Describe the morphology of the erythrocytes.
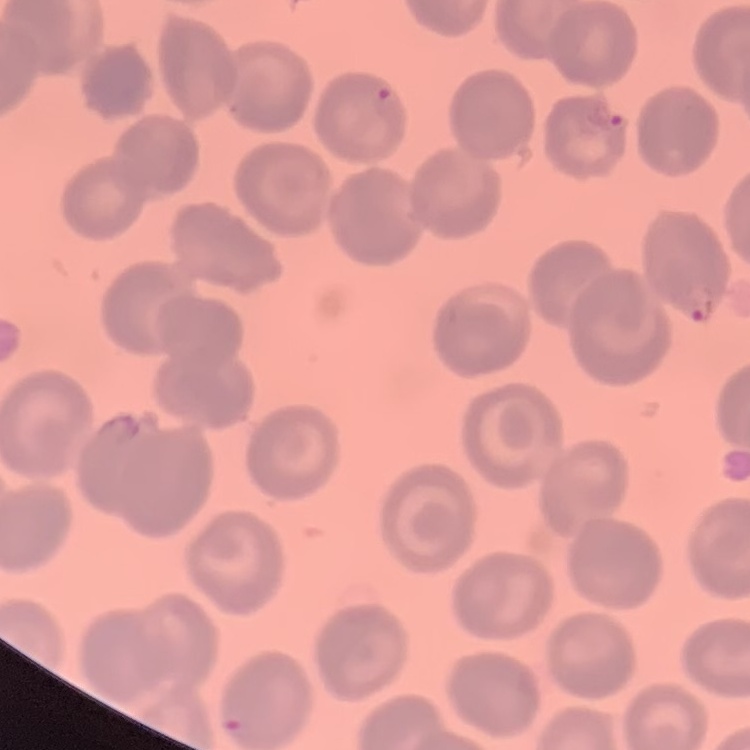
They show no rouleaux formation.

stain = Field's or Giemsa
preparation = thin peripheral smear
image type = one tile cut from a larger photomicrograph